Name the parasite shown.
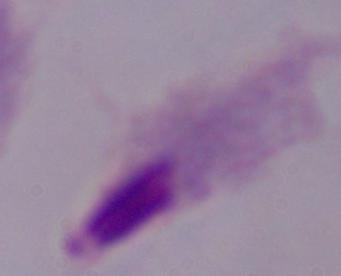
This is a trichomonad.

Captured at 1000x magnification. Photomicrograph.